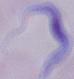

Photomicrograph. Captured at 1000x magnification. A trypanosome is seen.